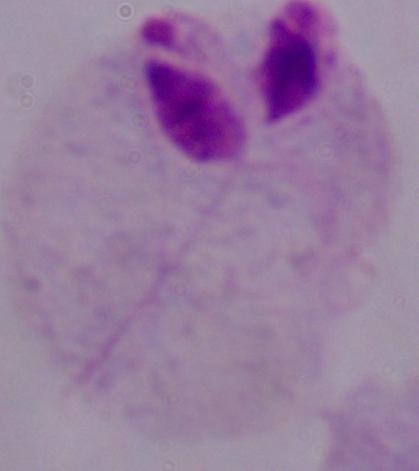 Micrograph. A trichomonad is shown. Captured at 1000x magnification.